Comment on the morphology of the red blood cells.
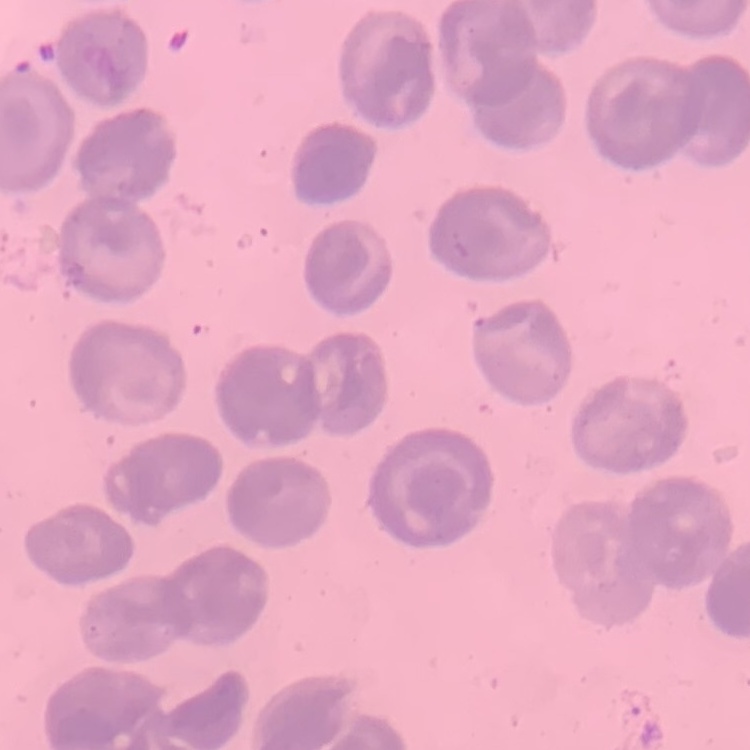

No rouleaux formation.

Summary:
  - Preparation: thin blood smear
  - Image type: square crop of a larger photomicrograph
  - Stain: Field's or Giemsa